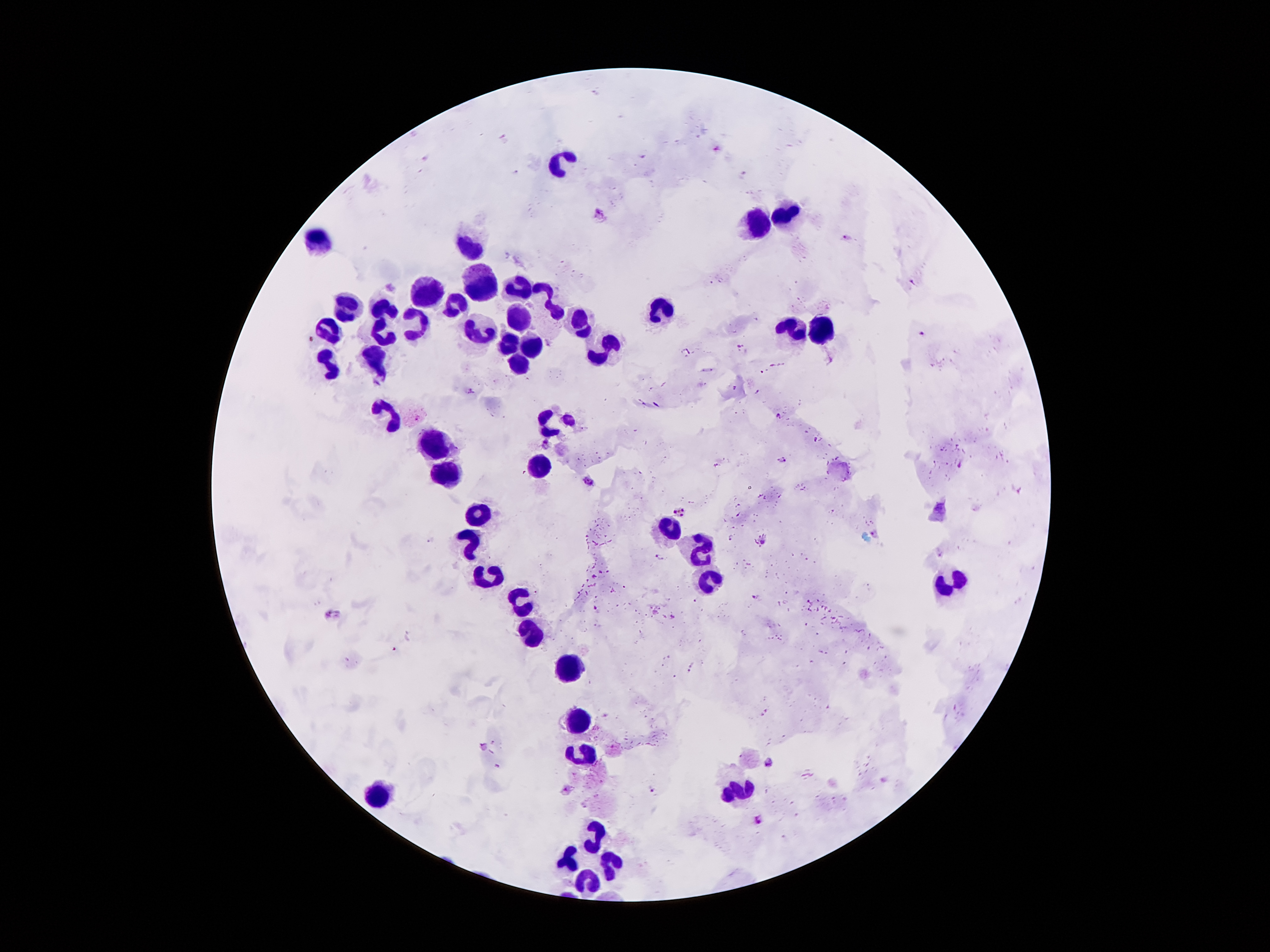

leukocyte_locations: 'approximate centers as {x, y} in pixels: {561, 158}, {786, 215}, {758, 226}, {314, 242}, {469, 246}, {477, 281}, {519, 288}, {428, 294}, {452, 303}, {348, 304}, {549, 304}, {660, 306}, {386, 308}, {519, 315}, {580, 318}, {415, 326}, {791, 330}, {823, 330}, {329, 331}, {479, 331}, {381, 336}, {504, 343}, {533, 345}, {603, 351}, {376, 355}, {517, 362}, {328, 363}, {388, 414}, {430, 445}, {541, 464}, {450, 476}, {480, 513}, {669, 528}, {472, 545}, {704, 551}, {489, 575}, {707, 580}, {951, 581}, {522, 602}, {529, 634}, {571, 665}, {583, 717}, {587, 753}, {739, 791}, {381, 795}, {591, 833}, {569, 855}, {613, 862}, {587, 879}'
preparation: thick blood smear
plasmodium_parasite_locations: 'approximate centers as {x, y} in pixels: {599, 212}, {844, 237}, {913, 282}, {924, 335}, {740, 346}, {688, 351}, {773, 365}, {761, 371}, {735, 389}, {472, 392}, {758, 392}, {778, 417}, {545, 441}, {783, 461}, {959, 466}, {589, 481}, {679, 513}, {874, 534}, {430, 539}, {763, 543}, {661, 556}, {755, 597}, {329, 613}, {395, 649}, {483, 746}, {770, 762}, {566, 791}, {653, 792}, {757, 820}'
magnification: 100x
image_size: 1270×952 pixels
patient_malaria_status: infected with Plasmodium falciparum
capture: smartphone camera through the microscope eyepiece
field_of_view: single
stain: Giemsa